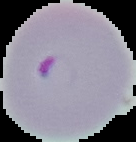

{
  "result": "Plasmodium parasites identified",
  "preparation": "thin blood smear",
  "image_size": "136×142 pixels",
  "image_type": "segmented cell region with the area outside set to black"
}